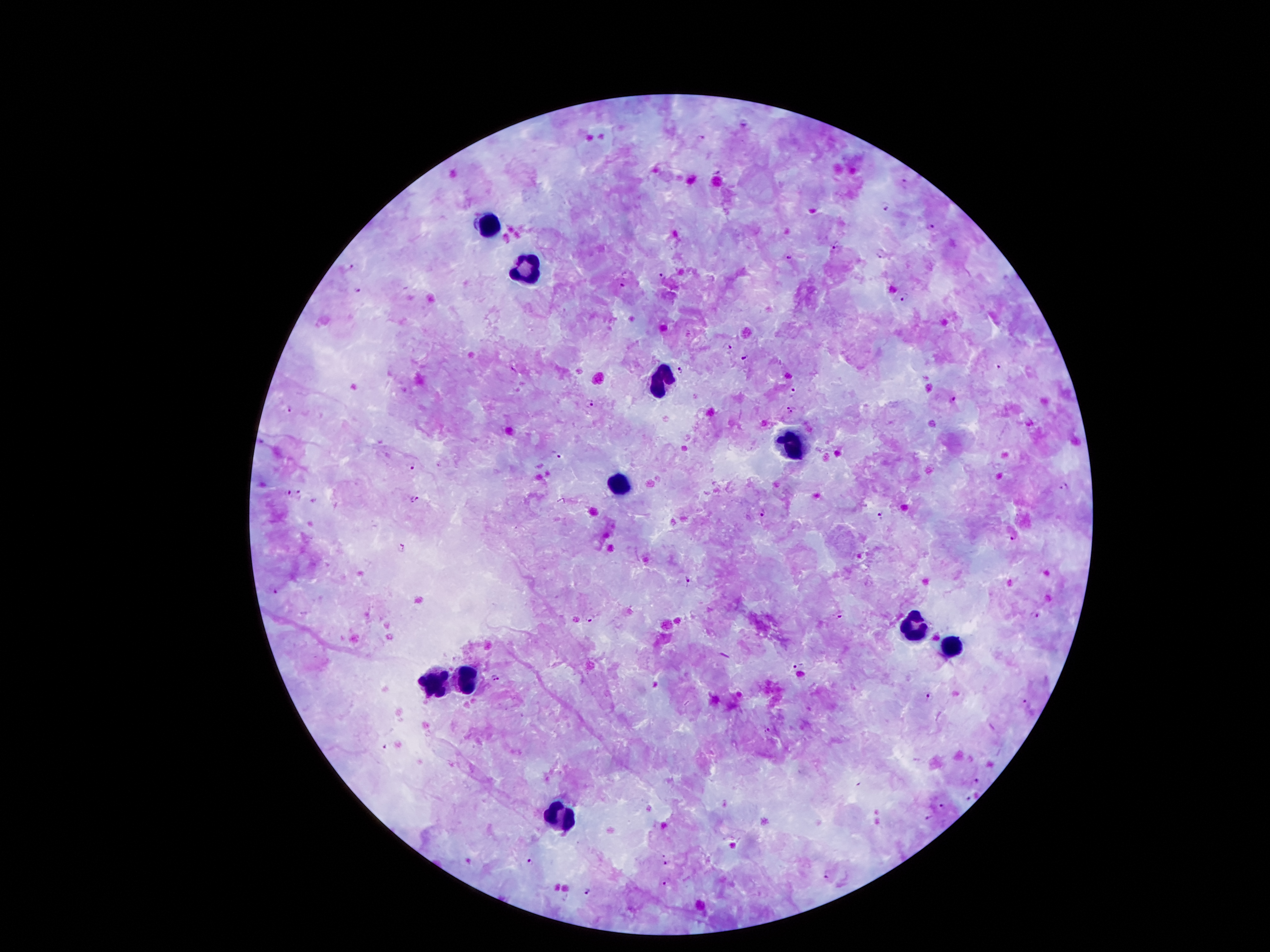
Approximate object centers, in pixels from the top-left corner. Malaria parasite locations: (x=703, y=138), (x=719, y=172), (x=905, y=184), (x=885, y=205), (x=929, y=225), (x=834, y=246), (x=879, y=254), (x=789, y=257), (x=350, y=265), (x=662, y=277), (x=622, y=285), (x=358, y=291), (x=905, y=298), (x=726, y=346), (x=746, y=356), (x=996, y=365), (x=515, y=370), (x=682, y=370), (x=793, y=394), (x=954, y=399), (x=589, y=404), (x=790, y=408), (x=288, y=410), (x=556, y=457), (x=411, y=466), (x=1064, y=488), (x=299, y=491), (x=288, y=493), (x=415, y=500), (x=764, y=512), (x=881, y=518), (x=1015, y=536), (x=401, y=548), (x=687, y=582), (x=275, y=592), (x=841, y=614), (x=1036, y=614), (x=592, y=619), (x=797, y=663), (x=495, y=678), (x=931, y=696), (x=1026, y=702), (x=767, y=729), (x=386, y=748), (x=976, y=781), (x=969, y=798), (x=943, y=806), (x=930, y=815), (x=529, y=861), (x=666, y=862), (x=826, y=875), (x=667, y=881), (x=587, y=891). Leukocyte locations: (x=489, y=225), (x=526, y=270), (x=657, y=379), (x=789, y=446), (x=624, y=485), (x=912, y=625), (x=954, y=645), (x=470, y=678), (x=439, y=684), (x=565, y=818). Patient malaria status: positive for Plasmodium falciparum. Thick peripheral-blood smear. Giemsa-stained preparation. Photographed through the microscope eyepiece with a smartphone camera. Image is 1270×952 pixels. 100x magnification. One field from this slide.